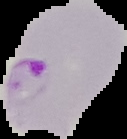

Summary:
  - Preparation: thin blood film
  - Malaria status: parasitized
  - Image type: segmented cell region with the area outside set to black
  - Image size: 127×139 pixels